Name the cell type shown.
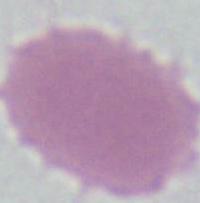
This is an erythrocyte.

modality = photomicrograph
magnification = 1000x